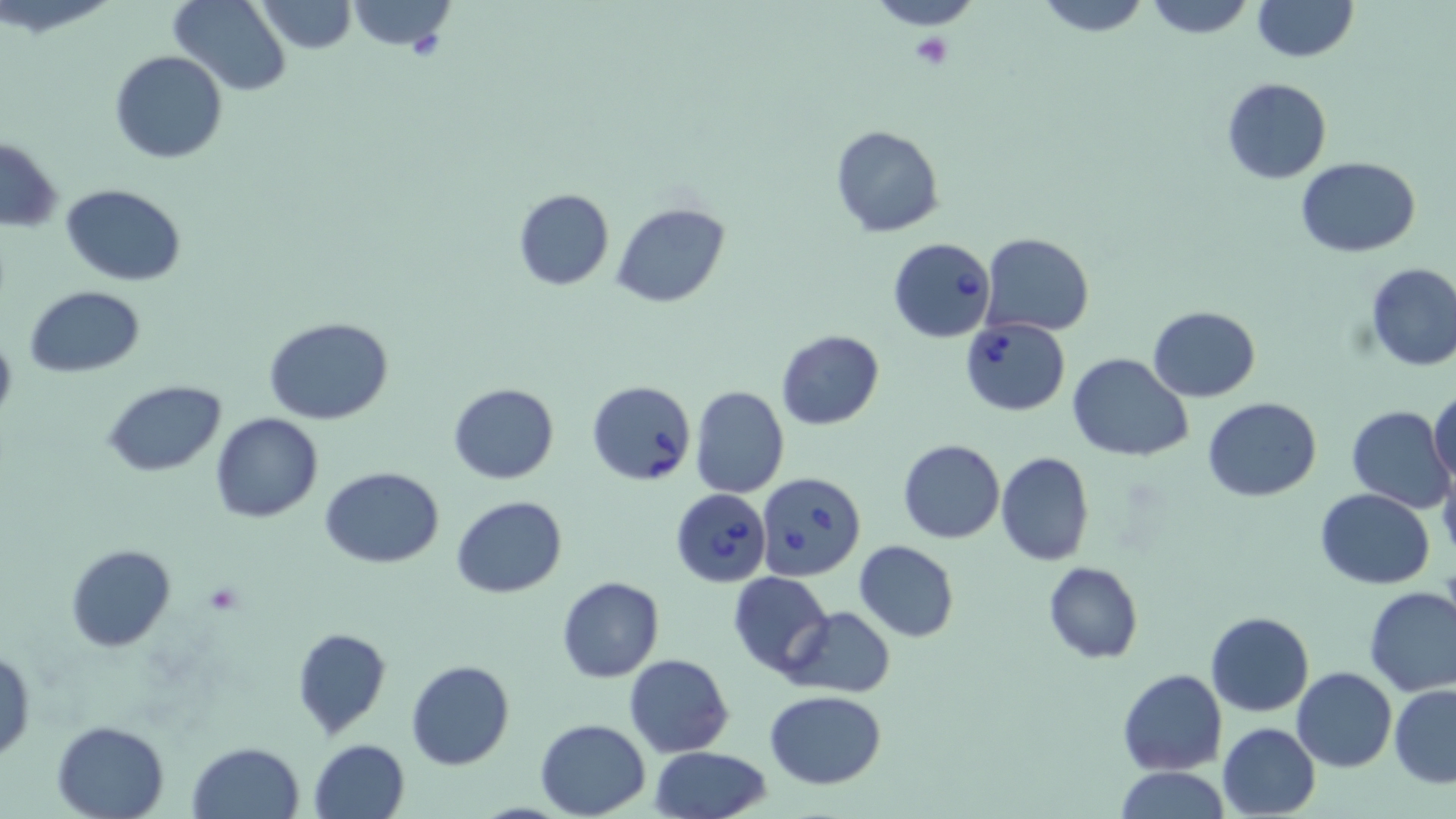
Approximate bounding boxes as named x1/y1/x2/y2 corners in pixels. Uninfected red blood cell locations: (x1=169, y1=0, x2=291, y2=96), (x1=253, y1=0, x2=357, y2=53), (x1=345, y1=0, x2=456, y2=53), (x1=863, y1=0, x2=988, y2=30), (x1=1033, y1=0, x2=1152, y2=37), (x1=1142, y1=0, x2=1255, y2=39), (x1=1248, y1=0, x2=1359, y2=62), (x1=109, y1=49, x2=228, y2=164), (x1=1222, y1=78, x2=1331, y2=184), (x1=830, y1=125, x2=944, y2=238), (x1=1, y1=137, x2=64, y2=232), (x1=1296, y1=158, x2=1421, y2=256), (x1=61, y1=183, x2=186, y2=286), (x1=512, y1=188, x2=614, y2=291), (x1=611, y1=201, x2=729, y2=308), (x1=979, y1=233, x2=1094, y2=337), (x1=1364, y1=262, x2=1456, y2=372), (x1=25, y1=286, x2=146, y2=377), (x1=1148, y1=304, x2=1260, y2=400), (x1=264, y1=316, x2=395, y2=424), (x1=0, y1=327, x2=17, y2=428), (x1=776, y1=330, x2=884, y2=429), (x1=1067, y1=352, x2=1193, y2=463), (x1=103, y1=379, x2=227, y2=477), (x1=449, y1=382, x2=559, y2=484), (x1=690, y1=385, x2=789, y2=498), (x1=1430, y1=393, x2=1456, y2=487), (x1=1205, y1=397, x2=1321, y2=502), (x1=1345, y1=405, x2=1452, y2=512), (x1=210, y1=414, x2=324, y2=523), (x1=897, y1=439, x2=1004, y2=543), (x1=994, y1=450, x2=1095, y2=567), (x1=1438, y1=457, x2=1456, y2=563), (x1=321, y1=467, x2=443, y2=568), (x1=1317, y1=488, x2=1435, y2=589), (x1=450, y1=495, x2=567, y2=599), (x1=854, y1=539, x2=959, y2=641), (x1=66, y1=543, x2=176, y2=651), (x1=1043, y1=561, x2=1142, y2=664), (x1=728, y1=570, x2=834, y2=677), (x1=558, y1=576, x2=664, y2=683), (x1=1363, y1=585, x2=1456, y2=698), (x1=786, y1=606, x2=895, y2=697), (x1=1206, y1=612, x2=1314, y2=717), (x1=292, y1=626, x2=390, y2=739), (x1=0, y1=647, x2=35, y2=766), (x1=624, y1=653, x2=734, y2=756), (x1=405, y1=660, x2=515, y2=770), (x1=1292, y1=667, x2=1396, y2=771), (x1=1119, y1=669, x2=1225, y2=775), (x1=1390, y1=684, x2=1456, y2=786), (x1=767, y1=691, x2=886, y2=788), (x1=51, y1=719, x2=171, y2=818), (x1=534, y1=719, x2=652, y2=818), (x1=1218, y1=723, x2=1321, y2=817), (x1=308, y1=738, x2=410, y2=819), (x1=188, y1=741, x2=305, y2=819), (x1=650, y1=747, x2=772, y2=819), (x1=1113, y1=766, x2=1231, y2=819). Platelet locations: (x1=909, y1=33, x2=955, y2=70), (x1=204, y1=581, x2=245, y2=614). Babesia divergens-infected red blood cell locations: (x1=887, y1=237, x2=996, y2=342), (x1=961, y1=318, x2=1070, y2=415), (x1=586, y1=380, x2=697, y2=486), (x1=756, y1=470, x2=866, y2=582), (x1=671, y1=488, x2=771, y2=587). Slide-level diagnosis: Babesia divergens. One field of a larger specimen. Image is 1456×819 pixels. Thin blood film. Optical microscopy. May-Grünwald-Giemsa stain. Captured at 1000x magnification.